Describe the morphology of the red blood cells.
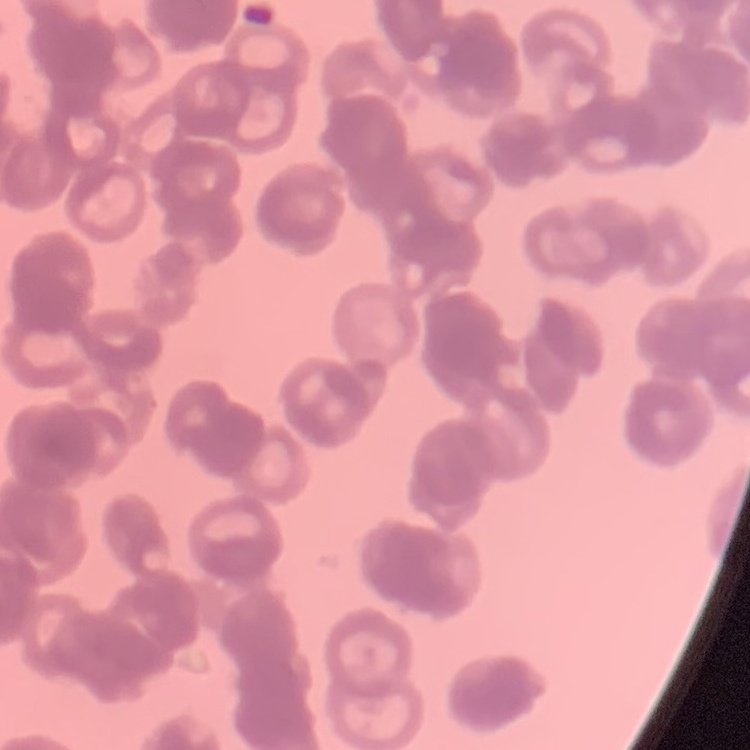
They show rouleaux formation.

Square crop of a larger photomicrograph. Thin peripheral smear. Stained with either Field's or Giemsa.